Locate every blood parasite and identify its species.
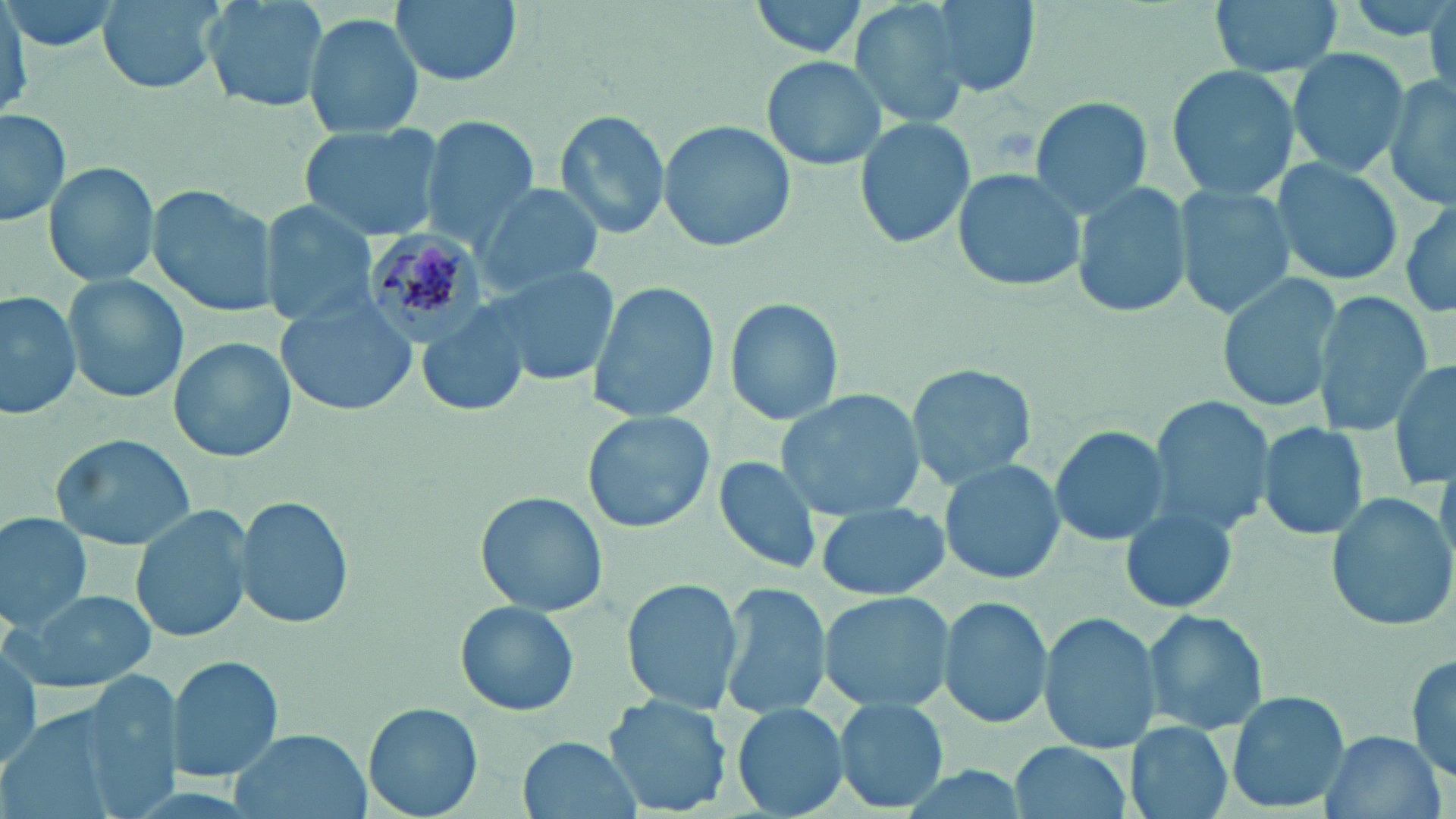

Approximate bounding boxes as named x1/y1/x2/y2 corners in pixels.
Plasmodium malariae-infected red blood cells: (x1=362, y1=229, x2=484, y2=342).
No Plasmodium falciparum, Plasmodium ovale, Plasmodium vivax, Babesia divergens, or Trypanosoma brucei observed.

Uninfected red blood cell locations: (x1=3, y1=0, x2=120, y2=56), (x1=97, y1=0, x2=224, y2=94), (x1=197, y1=0, x2=328, y2=114), (x1=389, y1=0, x2=520, y2=87), (x1=924, y1=0, x2=1041, y2=99), (x1=1210, y1=0, x2=1344, y2=79), (x1=0, y1=1, x2=32, y2=114), (x1=748, y1=1, x2=870, y2=61), (x1=846, y1=1, x2=979, y2=127), (x1=1426, y1=2, x2=1456, y2=97), (x1=303, y1=12, x2=424, y2=136), (x1=1285, y1=46, x2=1409, y2=179), (x1=761, y1=56, x2=889, y2=170), (x1=1166, y1=62, x2=1298, y2=202), (x1=1386, y1=77, x2=1456, y2=212), (x1=1027, y1=96, x2=1156, y2=218), (x1=0, y1=108, x2=72, y2=228), (x1=553, y1=108, x2=669, y2=241), (x1=422, y1=114, x2=540, y2=246), (x1=854, y1=118, x2=977, y2=251), (x1=658, y1=121, x2=796, y2=253), (x1=296, y1=122, x2=444, y2=242), (x1=1273, y1=157, x2=1406, y2=287), (x1=43, y1=161, x2=160, y2=287), (x1=949, y1=167, x2=1085, y2=293), (x1=1073, y1=179, x2=1195, y2=323), (x1=1173, y1=183, x2=1291, y2=322), (x1=477, y1=184, x2=605, y2=292), (x1=148, y1=185, x2=277, y2=319), (x1=260, y1=201, x2=378, y2=329), (x1=1399, y1=203, x2=1456, y2=318), (x1=485, y1=263, x2=621, y2=391), (x1=1216, y1=270, x2=1340, y2=415), (x1=62, y1=273, x2=189, y2=403), (x1=587, y1=278, x2=719, y2=424), (x1=0, y1=289, x2=81, y2=419), (x1=1313, y1=292, x2=1429, y2=435), (x1=276, y1=296, x2=419, y2=418), (x1=725, y1=296, x2=844, y2=428), (x1=417, y1=305, x2=529, y2=419), (x1=170, y1=338, x2=295, y2=463), (x1=1390, y1=357, x2=1456, y2=490), (x1=906, y1=360, x2=1039, y2=489), (x1=775, y1=389, x2=925, y2=520), (x1=1153, y1=396, x2=1276, y2=537), (x1=583, y1=409, x2=714, y2=534), (x1=1257, y1=422, x2=1371, y2=541), (x1=1050, y1=425, x2=1167, y2=547), (x1=50, y1=434, x2=195, y2=550), (x1=713, y1=457, x2=829, y2=576), (x1=942, y1=460, x2=1063, y2=583), (x1=1324, y1=490, x2=1455, y2=631), (x1=475, y1=491, x2=607, y2=617), (x1=235, y1=493, x2=352, y2=631), (x1=815, y1=501, x2=950, y2=602), (x1=130, y1=506, x2=254, y2=647), (x1=1122, y1=506, x2=1236, y2=614), (x1=0, y1=513, x2=92, y2=632), (x1=622, y1=576, x2=742, y2=716), (x1=719, y1=581, x2=834, y2=719), (x1=11, y1=589, x2=158, y2=691), (x1=818, y1=589, x2=957, y2=713), (x1=938, y1=596, x2=1053, y2=729), (x1=453, y1=598, x2=581, y2=718), (x1=1143, y1=609, x2=1270, y2=735), (x1=1039, y1=611, x2=1162, y2=756), (x1=1408, y1=647, x2=1456, y2=784), (x1=0, y1=648, x2=45, y2=773), (x1=167, y1=655, x2=284, y2=782), (x1=1226, y1=691, x2=1349, y2=813), (x1=605, y1=694, x2=732, y2=816), (x1=835, y1=699, x2=951, y2=814), (x1=364, y1=702, x2=483, y2=819), (x1=731, y1=705, x2=848, y2=816), (x1=1126, y1=721, x2=1234, y2=819), (x1=1318, y1=729, x2=1442, y2=819), (x1=228, y1=730, x2=373, y2=818), (x1=517, y1=735, x2=645, y2=819), (x1=1009, y1=739, x2=1132, y2=819). Slide-level diagnosis: Plasmodium malariae. One field of a larger specimen. Image is 1456×819 pixels. Thin blood smear. Light microscopy. Captured at 1000x magnification. May-Grünwald-Giemsa stain.